Classify this cell by malaria status.
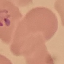
It is parasitized.

Summary:
  - Stain: Giemsa
  - Capture: smartphone camera at the microscope eyepiece
  - Image type: cell patch, automatically extracted from a larger field of view and resized to 64 × 64 pixels
  - Preparation: thin blood smear